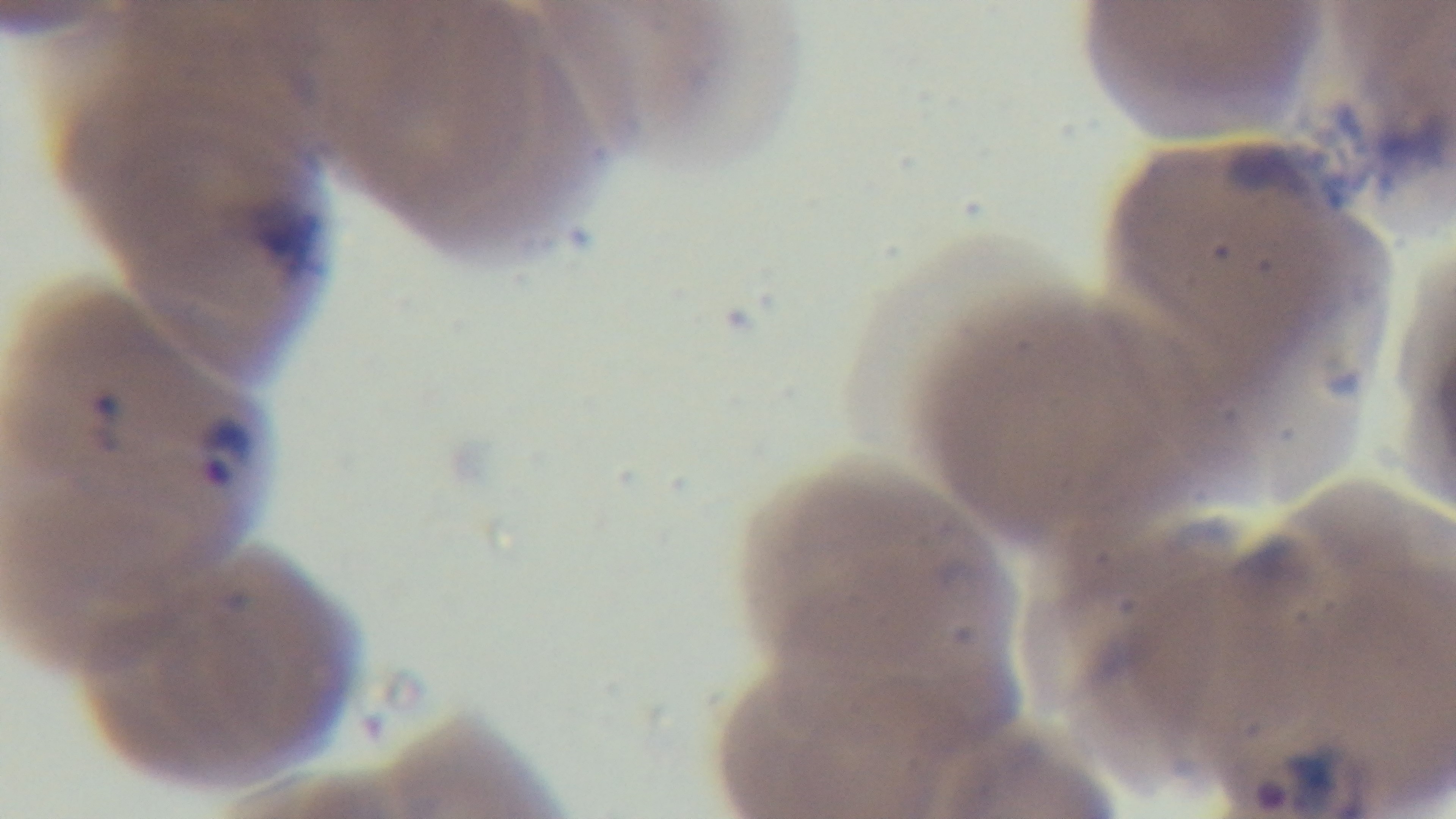

Summary:
  - Field of view: one from the slide
  - Preparation: thin blood film
  - Malaria status: positive
  - Objective: 100x oil immersion
  - Modality: light microscopy
  - Capture: mounted 4K digital camera
  - Stain: Giemsa